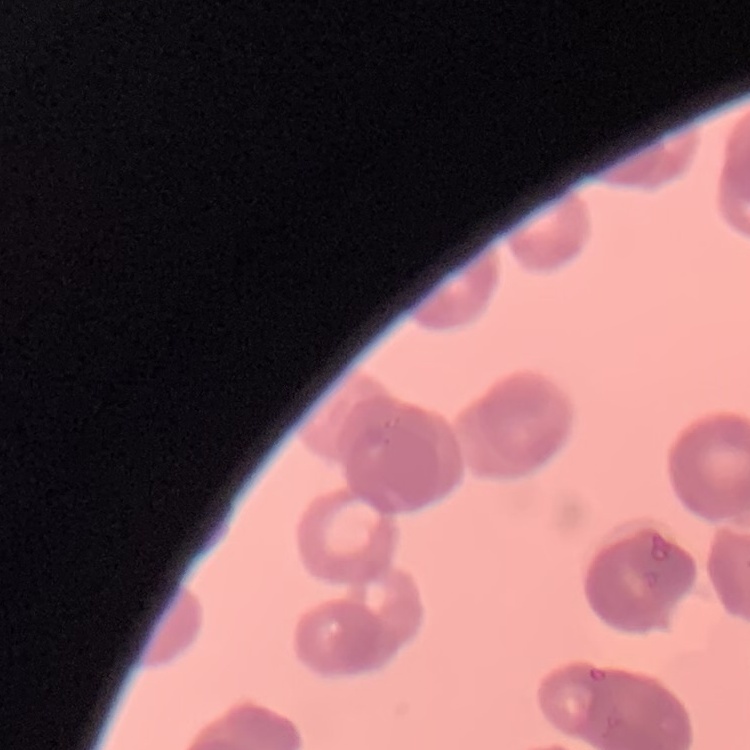
erythrocyte morphology = rouleaux formation
preparation = thin blood smear
image type = one tile cut from a larger photomicrograph
stain = Field's or Giemsa